Identify the parasite.
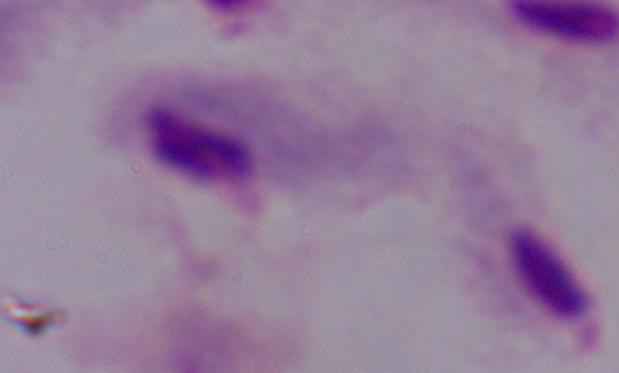
A trichomonad.

Summary:
  - Modality: photomicrograph
  - Magnification: 1000x